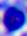

{
  "identification": "leukocyte",
  "magnification": "400x",
  "modality": "micrograph"
}